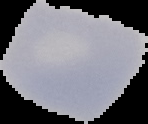 From a thin blood smear. Image is 148×124 pixels. Cell region segmented out of the field of view; the surrounding area is masked to black. Malaria status: uninfected.